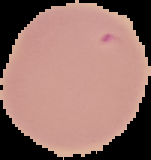

image size = 151×160 pixels
preparation = thin blood smear
result = no malaria parasites seen
image type = cell region segmented out of the field of view; surrounding area masked to black